Classify this cell by malaria status.
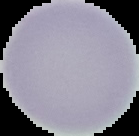
Uninfected.

{
  "image_size": "139×136 pixels",
  "image_type": "segmented cell region with the area outside set to black",
  "preparation": "thin blood film"
}